Give the position of every malaria parasite.
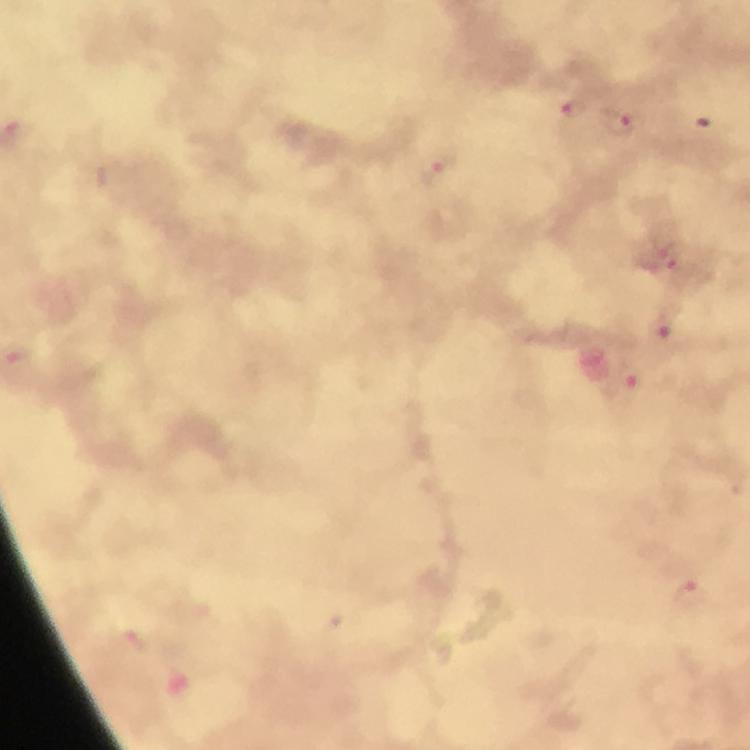
Approximate centers as [x, y] in pixels.
Malaria parasites: [574, 109], [627, 123], [437, 174], [667, 255], [662, 324], [630, 384], [688, 595].

Immersion oil applied. Thick smear. Image is 750×750 pixels. Photographed through the microscope with a smartphone camera. Giemsa stain. At 100x magnification. From a diagnostic examination for malaria. Cropped region of a single field of view.